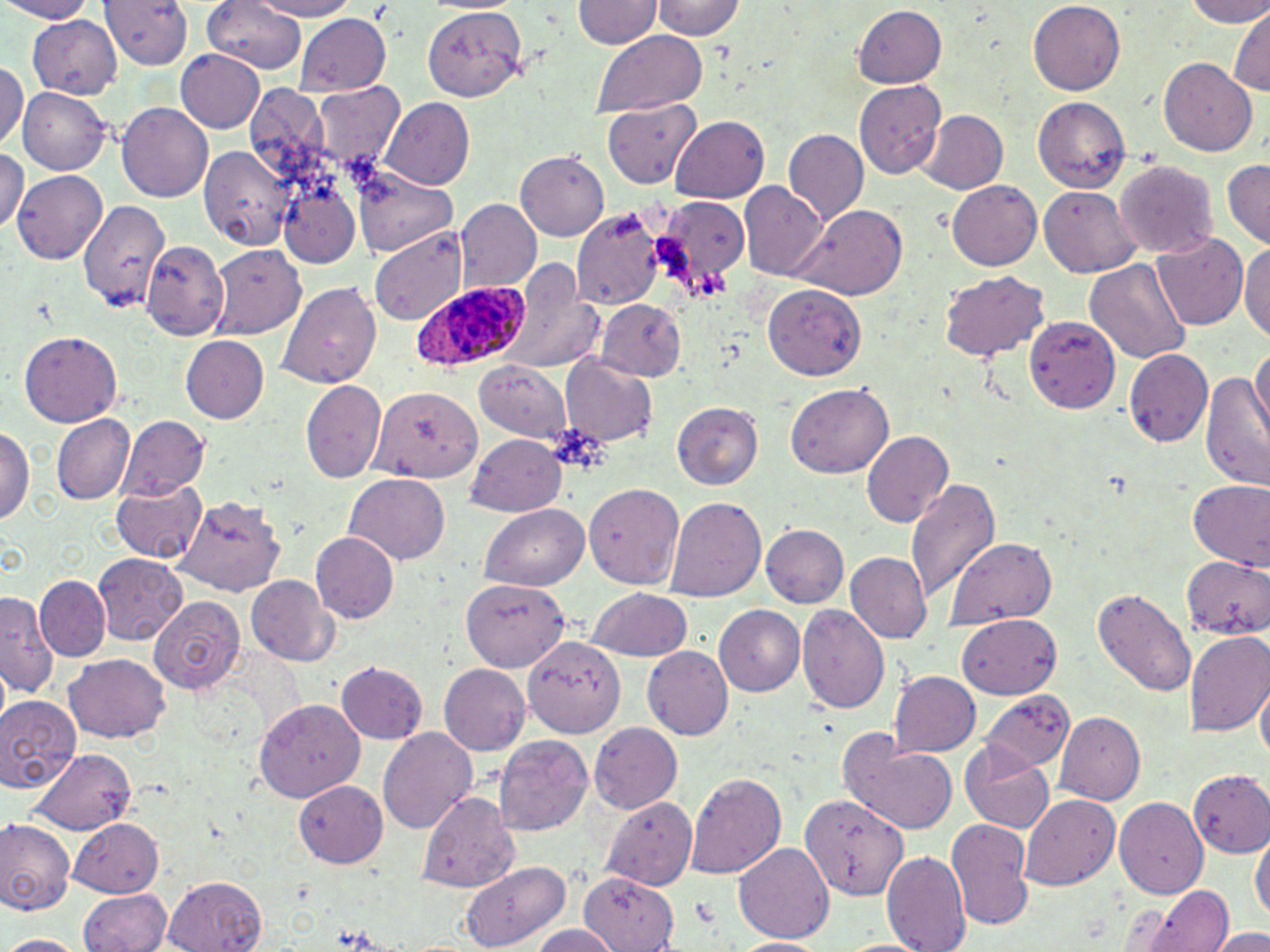

Approximate bounding boxes as (x1, y1, x2, y2) in pixels. Plasmodium ovale-infected red blood cell locations: (412, 283, 531, 373). Uninfected red blood cell locations: (0, 0, 96, 23), (97, 0, 195, 72), (200, 0, 309, 74), (251, 0, 357, 21), (575, 0, 659, 50), (650, 0, 744, 41), (1180, 0, 1270, 27), (1026, 2, 1126, 94), (853, 5, 946, 90), (422, 6, 527, 101), (1229, 8, 1268, 99), (294, 14, 390, 96), (26, 15, 119, 98), (592, 31, 707, 116), (175, 50, 266, 134), (1160, 60, 1257, 156), (0, 63, 26, 149), (855, 80, 946, 180), (312, 81, 404, 170), (242, 82, 336, 187), (20, 87, 111, 177), (1033, 98, 1129, 192), (380, 101, 474, 188), (600, 103, 704, 192), (117, 104, 212, 204), (920, 111, 1006, 194), (671, 115, 770, 203), (785, 131, 867, 226), (198, 146, 294, 251), (0, 147, 27, 232), (516, 152, 607, 239), (1221, 158, 1269, 247), (1113, 162, 1216, 260), (11, 170, 106, 263), (352, 170, 457, 257), (947, 181, 1041, 271), (741, 183, 830, 282), (1041, 187, 1138, 277), (277, 188, 364, 268), (657, 193, 747, 300), (77, 199, 170, 309), (456, 200, 541, 294), (783, 204, 911, 300), (573, 207, 669, 310), (371, 225, 465, 323), (1151, 233, 1246, 332), (1240, 238, 1270, 344), (141, 240, 230, 340), (210, 245, 307, 341), (1084, 256, 1190, 367), (502, 259, 599, 374), (940, 271, 1049, 362), (276, 281, 382, 388), (763, 285, 869, 374), (595, 300, 685, 380), (1027, 317, 1117, 410), (18, 330, 123, 426), (181, 337, 269, 423), (1251, 341, 1270, 443), (1124, 349, 1213, 446), (562, 356, 657, 447), (476, 360, 573, 442), (1201, 369, 1270, 488), (300, 379, 386, 484), (786, 384, 894, 480), (373, 386, 482, 482), (672, 402, 763, 488), (54, 416, 133, 503), (121, 416, 210, 499), (0, 426, 33, 530), (862, 429, 955, 528), (467, 433, 566, 518), (344, 475, 449, 563), (906, 478, 1001, 600), (110, 480, 207, 563), (1186, 480, 1268, 568), (582, 482, 685, 591), (667, 496, 766, 603), (176, 497, 283, 595), (481, 505, 590, 592), (760, 525, 847, 608), (311, 532, 400, 625), (946, 540, 1056, 628), (846, 552, 932, 643), (94, 554, 187, 645), (1180, 555, 1270, 641), (247, 576, 339, 665), (34, 577, 110, 660), (461, 579, 568, 672), (1091, 586, 1195, 698), (587, 588, 692, 662), (1, 592, 57, 703), (149, 596, 243, 693), (714, 605, 806, 696), (799, 605, 889, 717), (960, 614, 1060, 698), (1186, 629, 1270, 737), (524, 634, 626, 737), (643, 646, 733, 743), (62, 654, 172, 743), (338, 661, 428, 742), (439, 664, 530, 757), (890, 673, 979, 755), (1258, 682, 1269, 772), (981, 694, 1074, 777), (0, 695, 81, 793), (253, 699, 363, 802), (1055, 711, 1146, 804), (591, 723, 681, 815), (377, 728, 478, 836), (495, 733, 591, 836), (846, 737, 961, 836), (961, 744, 1056, 832), (27, 748, 137, 835), (1186, 772, 1270, 855), (686, 773, 787, 879), (295, 778, 388, 864), (417, 789, 519, 892), (1021, 793, 1120, 886), (599, 797, 694, 888), (1118, 797, 1209, 901), (799, 801, 905, 897), (67, 818, 165, 897), (1, 819, 75, 916), (946, 819, 1035, 930), (1252, 833, 1268, 927), (734, 843, 834, 943), (884, 846, 972, 952), (460, 860, 570, 948), (167, 872, 266, 951), (579, 873, 678, 951), (1140, 882, 1234, 952), (77, 890, 172, 952), (528, 923, 622, 952), (1213, 927, 1270, 952), (1, 934, 87, 952), (730, 936, 826, 951). Slide-level diagnosis: Plasmodium ovale. Captured at 1000x magnification. May-Grünwald-Giemsa-stained preparation. Optical microscopy. Single field of view. Thin blood film. Image is 1270×952 pixels.